Classify this cell by malaria status.
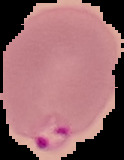

It is parasitized.

From a thin blood film. Segmented cell region on a black background. Image is 124×160 pixels.